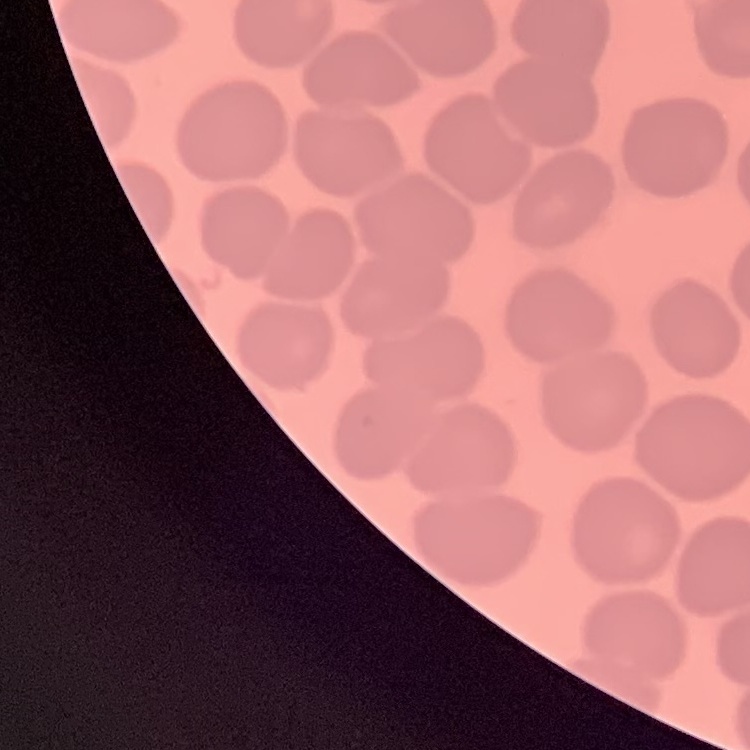
Summary:
  - Red blood cell morphology: no rouleaux formation
  - Stain: Field's or Giemsa
  - Image type: square crop of a larger photomicrograph
  - Preparation: thin blood film